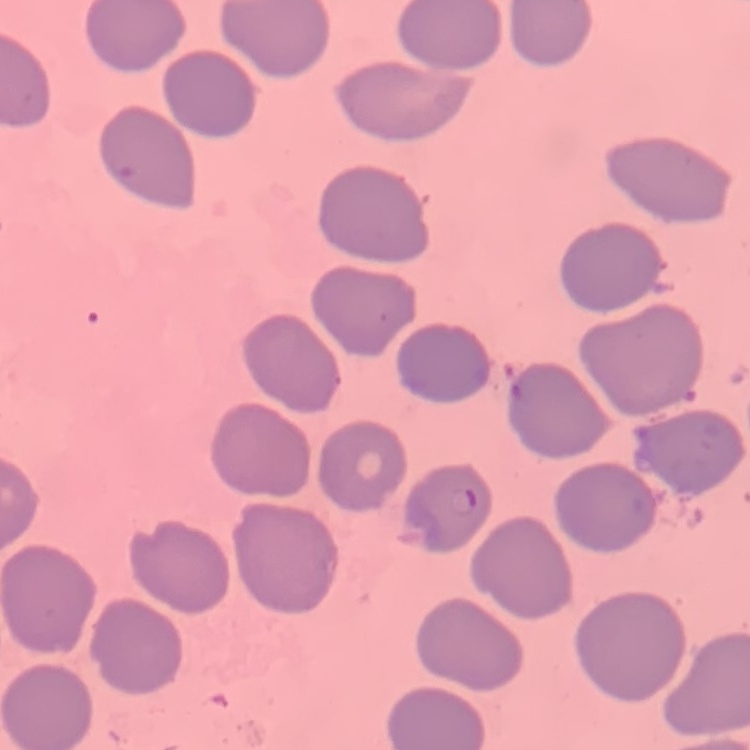

The red blood cells show no rouleaux formation. Field's or Giemsa stain. Thin blood smear. One tile cut from a larger photomicrograph.